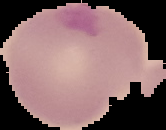

malaria status = parasitized
image type = cell region segmented out of the field of view; surrounding area masked to black
image size = 166×130 pixels
preparation = thin blood film